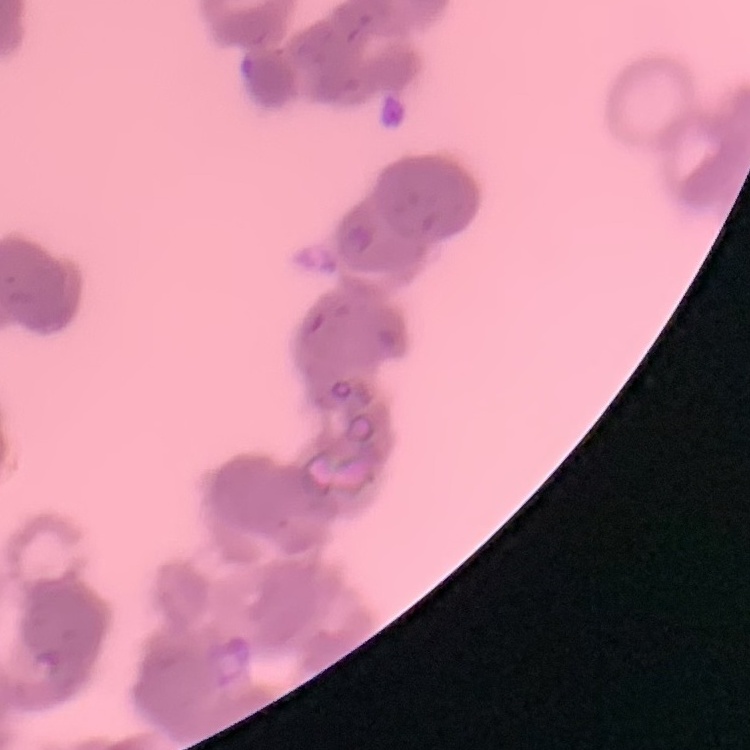

The red blood cells exhibit rouleaux formation. Thin peripheral smear. One tile cut from a larger photomicrograph. Field's or Giemsa stain.